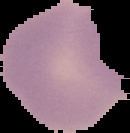
Summary:
  - Image type: cell region segmented out of the field of view; surrounding area masked to black
  - Malaria status: uninfected
  - Preparation: thin blood film
  - Image size: 130×133 pixels